Outline each blood parasite and name the species.
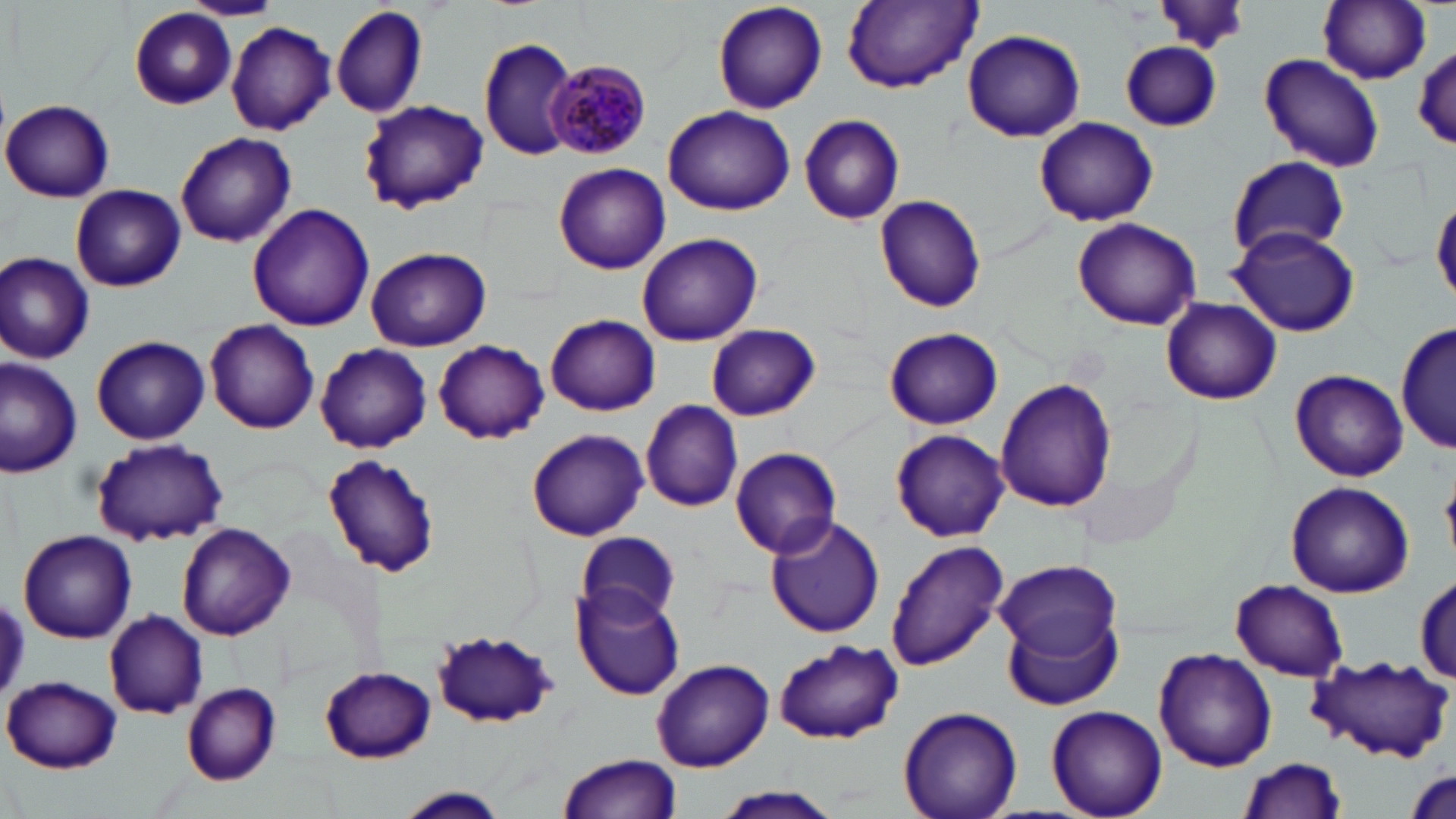

Approximate bounding boxes as (x1, y1, x2, y2) in pixels.
Plasmodium malariae-infected red blood cells: (548, 60, 654, 159).
No Plasmodium falciparum, Plasmodium ovale, Plasmodium vivax, Babesia divergens, or Trypanosoma brucei observed.

Summary:
  - Uninfected red blood cell locations: (180, 0, 284, 21), (711, 1, 826, 114), (1317, 1, 1431, 85), (842, 2, 982, 92), (331, 3, 428, 118), (128, 6, 237, 111), (226, 21, 336, 136), (961, 29, 1085, 143), (479, 38, 578, 161), (1120, 42, 1224, 131), (1413, 45, 1456, 150), (1257, 53, 1385, 173), (359, 99, 488, 214), (1, 100, 115, 202), (663, 105, 796, 217), (798, 112, 906, 224), (1033, 116, 1159, 227), (1044, 118, 1175, 324), (175, 133, 297, 248), (1224, 155, 1353, 261), (553, 163, 671, 275), (70, 183, 188, 292), (873, 195, 989, 312), (1431, 195, 1456, 304), (247, 204, 374, 332), (1070, 217, 1202, 331), (1228, 225, 1361, 338), (637, 232, 763, 347), (364, 246, 493, 350), (0, 252, 96, 364), (1160, 296, 1281, 405), (546, 314, 661, 416), (1396, 316, 1453, 456), (203, 319, 320, 434), (702, 324, 822, 420), (884, 327, 1004, 430), (90, 334, 210, 445), (434, 340, 549, 444), (315, 343, 432, 454), (0, 359, 82, 477), (1289, 369, 1408, 482), (995, 378, 1116, 512), (640, 400, 745, 511), (526, 427, 648, 541), (892, 429, 1011, 542), (89, 440, 229, 546), (730, 447, 844, 560), (321, 453, 440, 579), (1285, 481, 1414, 599), (765, 514, 886, 638), (175, 522, 296, 641), (577, 530, 681, 625), (18, 531, 136, 643), (884, 537, 1012, 671), (999, 559, 1121, 662), (1414, 573, 1455, 682), (573, 580, 686, 699), (1231, 580, 1349, 681), (1003, 609, 1124, 713), (103, 610, 209, 719), (431, 630, 561, 730), (775, 640, 902, 742), (1153, 647, 1276, 772), (1308, 653, 1452, 763), (652, 658, 774, 771), (318, 666, 436, 762), (2, 676, 125, 774), (181, 683, 282, 784), (1046, 705, 1166, 819), (898, 706, 1022, 819), (558, 754, 682, 819), (1236, 757, 1347, 818), (712, 786, 843, 819), (395, 787, 509, 818)
  - Slide-level diagnosis: Plasmodium malariae
  - Preparation: thin blood smear
  - Image size: 1456×819 pixels
  - Stain: May-Grünwald-Giemsa
  - Field of view: single
  - Magnification: 1000x
  - Modality: optical microscopy